State which cell type is depicted.
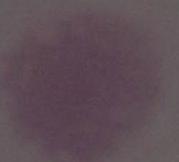

This is an erythrocyte.

magnification = 1000x
modality = photomicrograph